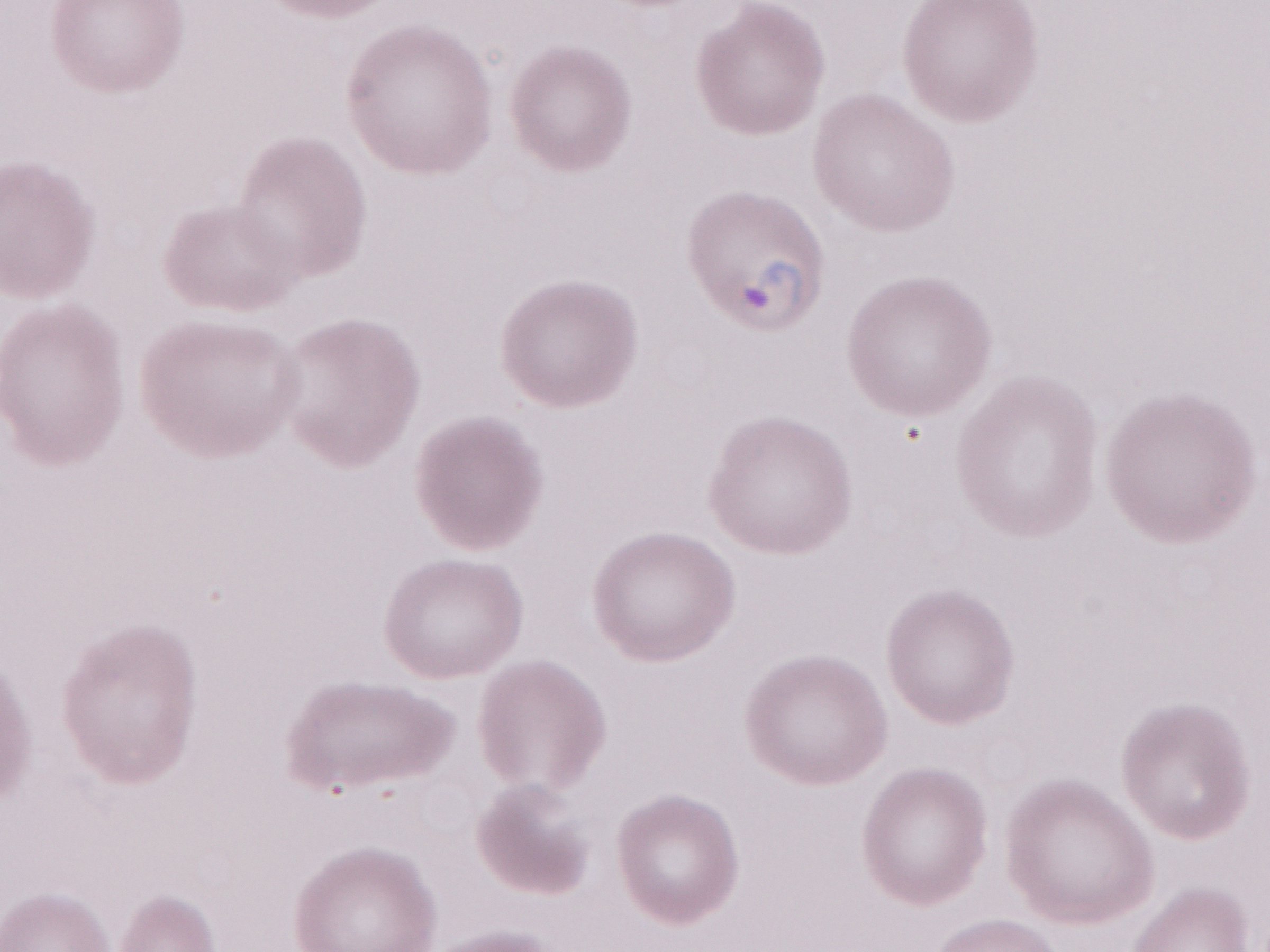
Image is 1270×952 pixels. 1,000x magnification. Thin peripheral-blood smear. One field of this slide. May-Grünwald-Giemsa stain. Malaria diagnosis (patient-level): positive. Olympus BX43 microscope, Olympus DP73 camera.